Find each parasitized RBC.
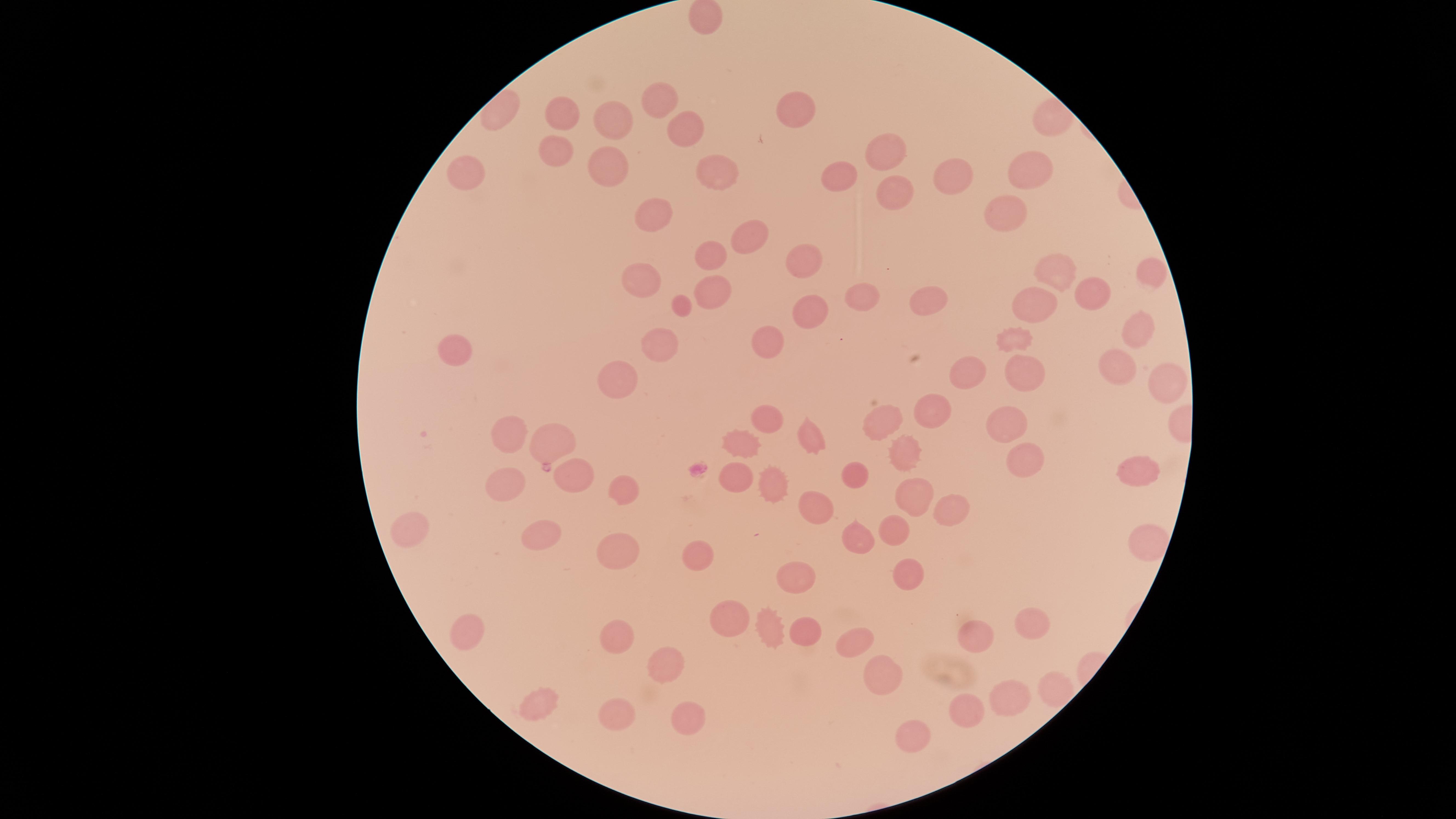
No parasitized RBCs identified.

{
  "image_size": "1456×819 pixels",
  "visible_region": "circular",
  "uninfected_RBCs": "approximate marker points as (x, y) in pixels: (662, 104), (797, 107), (564, 115), (618, 122), (683, 132), (556, 146), (887, 149), (1033, 164), (606, 166), (953, 171), (719, 175), (839, 178), (892, 191), (654, 216), (1009, 216), (748, 237), (711, 255), (800, 257), (1055, 270), (1150, 270), (645, 280), (1093, 292), (712, 294), (862, 298), (930, 300), (1033, 302), (684, 308), (813, 314), (1136, 328), (1018, 336), (662, 342), (456, 345), (769, 349), (966, 369), (1117, 369), (1026, 371), (619, 380), (1170, 384), (935, 415), (763, 416), (886, 420), (1006, 425), (510, 429), (553, 437), (811, 437), (736, 442), (905, 450), (1019, 461), (1140, 471), (852, 473), (573, 478), (735, 479), (506, 482), (623, 485), (773, 486), (911, 494), (812, 504), (948, 512), (417, 524), (897, 532), (853, 538), (538, 539), (618, 553), (696, 556), (910, 571), (798, 578), (734, 619), (1031, 622), (803, 623), (766, 624), (470, 625), (616, 636), (980, 636), (854, 641), (670, 664), (883, 673), (1053, 687), (1010, 698), (535, 702), (969, 707), (619, 711), (688, 716), (917, 733)",
  "field_of_view": "single",
  "stain": "Giemsa",
  "capture": "smartphone photograph through the microscope eyepiece",
  "preparation": "thin blood smear"
}